Locate every blood parasite and identify its species.
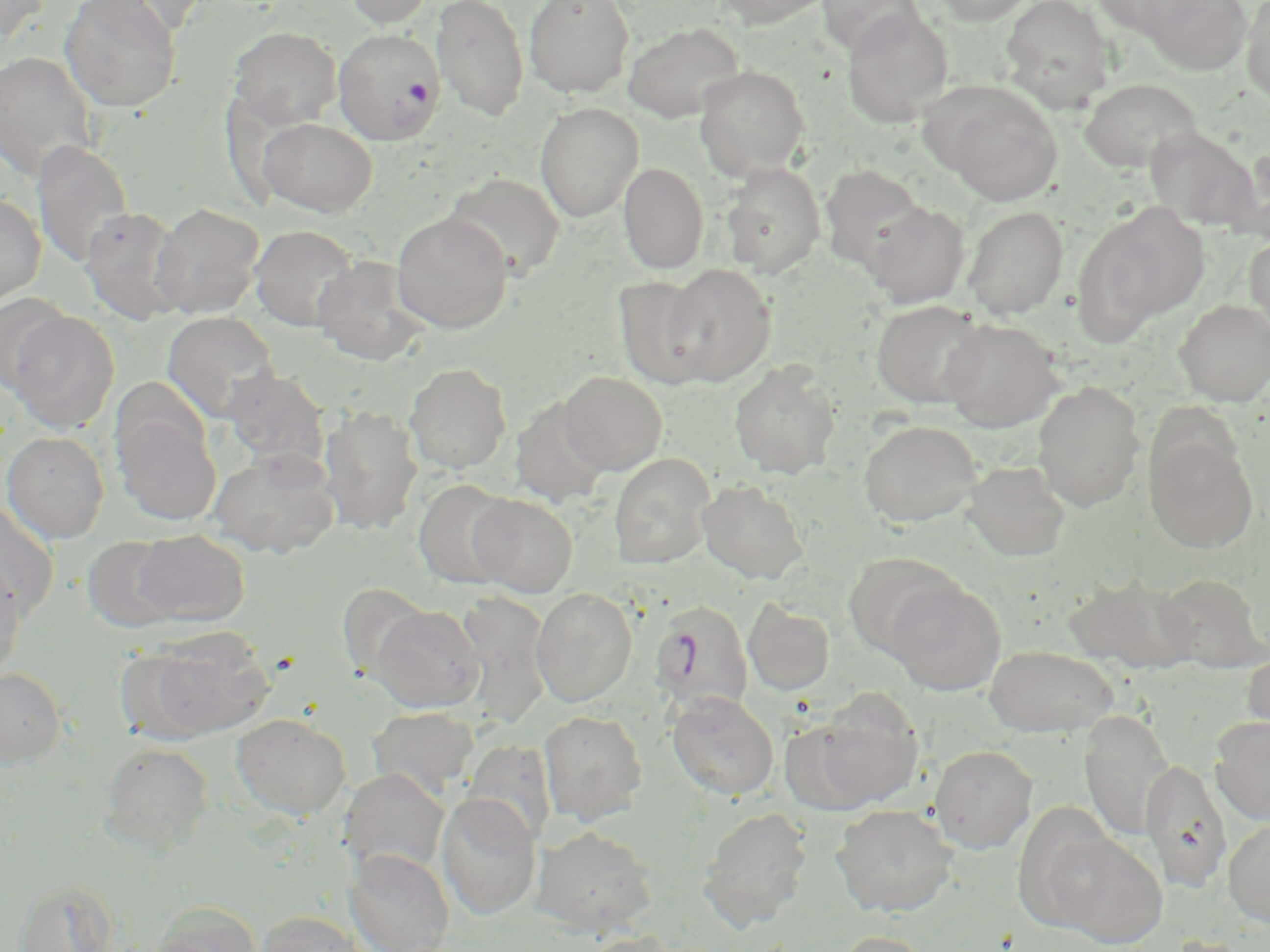

Approximate bounding boxes as (x1, y1, x2, y2) in pixels.
Plasmodium falciparum-infected red blood cells: (332, 28, 444, 143), (651, 600, 754, 714).
No Plasmodium ovale, Plasmodium malariae, Plasmodium vivax, Babesia divergens, or Trypanosoma brucei observed.

Uninfected red blood cell locations: (87, 0, 212, 36), (344, 0, 434, 28), (431, 0, 529, 121), (524, 0, 634, 97), (709, 0, 836, 28), (816, 0, 924, 57), (930, 0, 1036, 25), (1000, 0, 1115, 112), (1088, 0, 1200, 36), (1140, 0, 1253, 75), (1241, 0, 1270, 105), (0, 1, 50, 45), (60, 1, 181, 114), (842, 7, 953, 127), (623, 22, 744, 122), (228, 27, 341, 131), (0, 51, 98, 181), (693, 66, 810, 180), (1079, 78, 1202, 173), (931, 84, 1065, 206), (534, 102, 643, 222), (257, 117, 377, 216), (1145, 128, 1262, 233), (31, 139, 134, 268), (1227, 147, 1270, 243), (720, 162, 826, 279), (618, 163, 709, 273), (819, 165, 926, 271), (443, 173, 566, 279), (0, 193, 46, 306), (1075, 201, 1209, 337), (150, 202, 264, 319), (861, 202, 971, 308), (962, 206, 1069, 319), (79, 208, 187, 324), (392, 212, 513, 334), (249, 225, 361, 332), (1245, 233, 1270, 342), (312, 255, 431, 366), (662, 264, 775, 386), (613, 275, 717, 389), (1, 293, 71, 392), (1173, 299, 1270, 405), (872, 300, 989, 408), (5, 310, 121, 433), (162, 311, 280, 422), (940, 319, 1064, 433), (729, 360, 841, 480), (405, 363, 511, 474), (220, 368, 330, 472), (559, 371, 667, 475), (1032, 382, 1145, 512), (510, 397, 611, 508), (319, 405, 423, 535), (112, 406, 222, 527), (858, 420, 982, 528), (1, 431, 109, 543), (1145, 434, 1259, 553), (208, 447, 340, 559), (609, 453, 715, 569), (962, 461, 1071, 561), (413, 479, 518, 589), (697, 480, 809, 584), (467, 494, 578, 596), (0, 499, 59, 624), (133, 531, 249, 625), (82, 536, 182, 632), (843, 552, 963, 660), (0, 558, 28, 683), (1064, 571, 1198, 675), (1155, 573, 1267, 672), (885, 578, 1006, 695), (336, 582, 432, 680), (531, 588, 637, 707), (455, 591, 553, 727), (743, 600, 835, 695), (371, 605, 485, 713), (134, 628, 274, 742), (985, 645, 1118, 737), (1241, 648, 1270, 743), (0, 668, 67, 768), (668, 691, 779, 800), (800, 695, 924, 810), (368, 706, 479, 799), (539, 709, 647, 825), (1079, 709, 1174, 842), (231, 714, 351, 820), (1209, 716, 1270, 825), (98, 742, 214, 856), (929, 744, 1037, 853), (1140, 759, 1233, 891), (339, 768, 450, 876), (436, 792, 542, 920), (831, 804, 958, 917), (698, 807, 812, 929), (1223, 819, 1270, 926), (532, 826, 656, 936), (1045, 831, 1167, 947), (344, 848, 455, 952), (13, 879, 121, 952), (149, 901, 262, 952), (254, 910, 369, 952), (574, 931, 684, 952), (829, 931, 936, 952). Slide-level diagnosis: Plasmodium falciparum. Thin blood smear. Optical microscopy. 1000x magnification. May-Grünwald-Giemsa stain. Image is 1270×952 pixels. One field of a larger specimen.